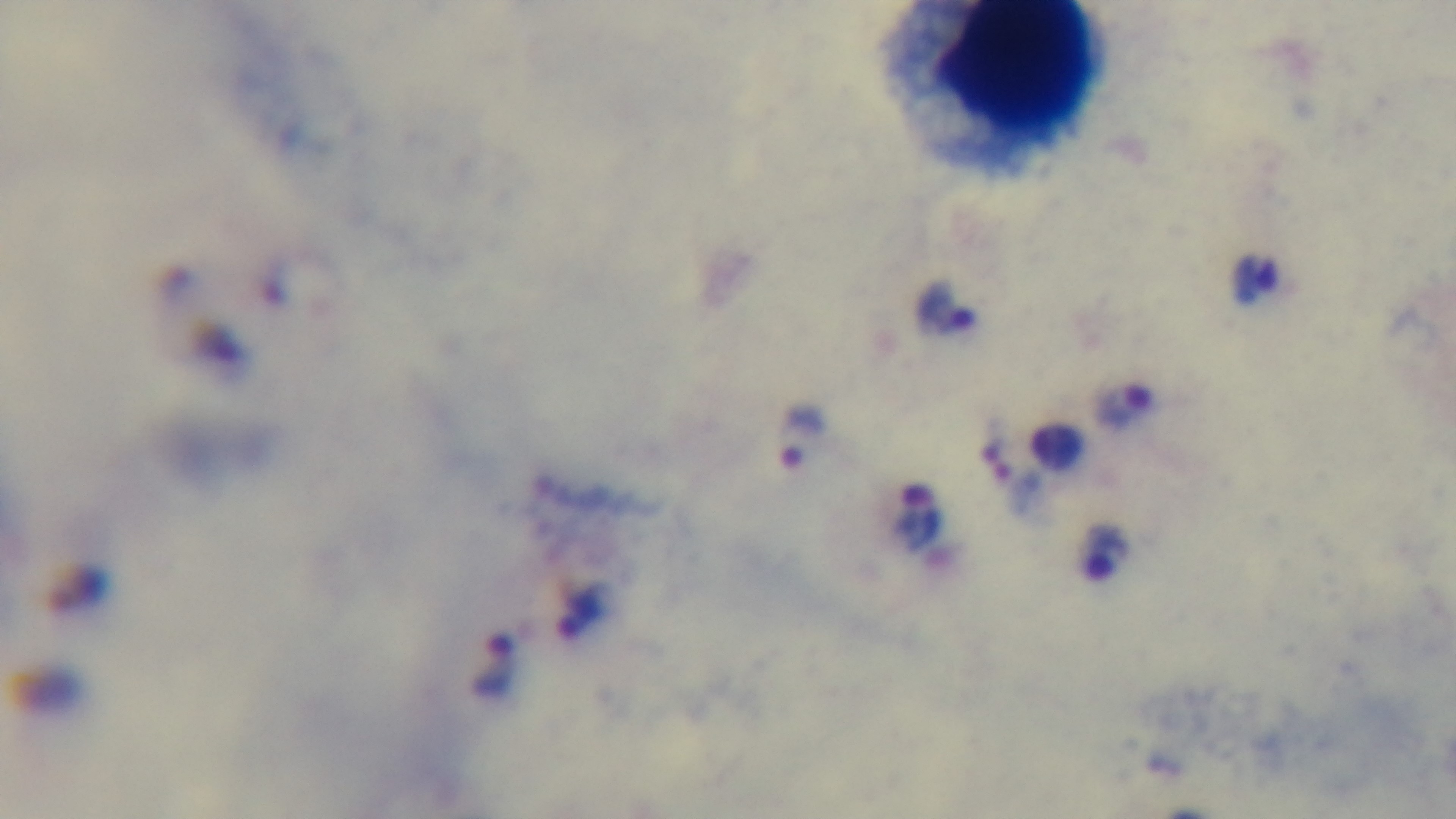
objective: 100x oil immersion
capture: mounted 4K digital camera
field_of_view: single
malaria_status: positive
preparation: thick blood film
stain: Giemsa
modality: light microscopy